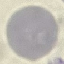
Malaria status: uninfected. Giemsa-stained preparation. Cell patch, automatically extracted from a larger field of view and resized to 64 × 64 pixels. Thin blood film. Acquired by smartphone through the microscope eyepiece.